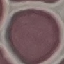
Summary:
  - Malaria status: uninfected
  - Preparation: thin blood film
  - Image type: automatically extracted cell patch, resized to 64 × 64 pixels
  - Capture: smartphone camera at the microscope eyepiece
  - Stain: Giemsa